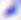

400x magnification. Toxoplasma gondii is seen. Photomicrograph.